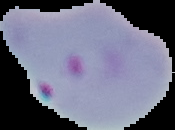

Summary:
  - Preparation: thin blood smear
  - Image size: 175×130 pixels
  - Malaria status: parasitized
  - Image type: cell region segmented out of the field of view; surrounding area masked to black